Classify this cell by malaria status.
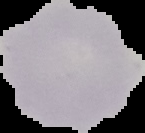
Uninfected.

image type = segmented cell region on a black background
image size = 145×133 pixels
preparation = thin blood smear